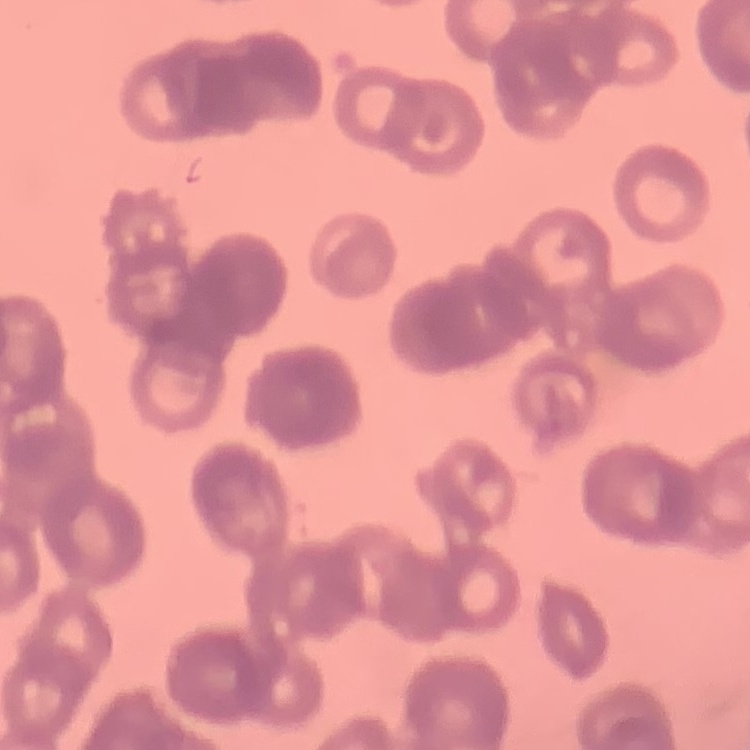
{
  "red_blood_cell_morphology": "rouleaux formation",
  "image_type": "one tile cut from a larger photomicrograph",
  "preparation": "thin peripheral smear",
  "stain": "Field's or Giemsa"
}